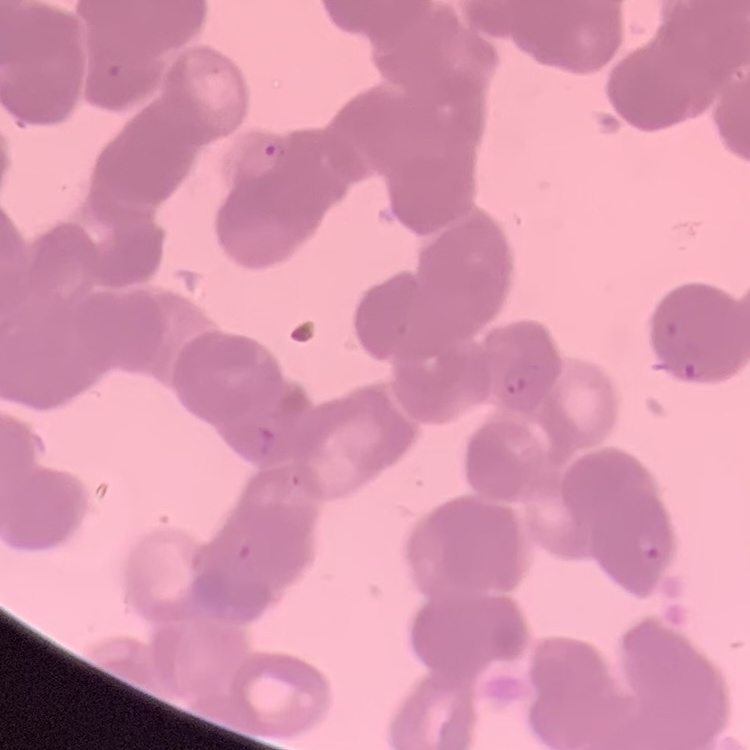

{
  "red_blood_cell_morphology": "rouleaux formation",
  "stain": "Field's or Giemsa",
  "preparation": "thin blood smear",
  "image_type": "square crop of a larger photomicrograph"
}